Identify the cell.
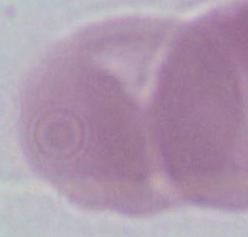

An erythrocyte.

Photomicrograph. Captured at 1000x magnification.